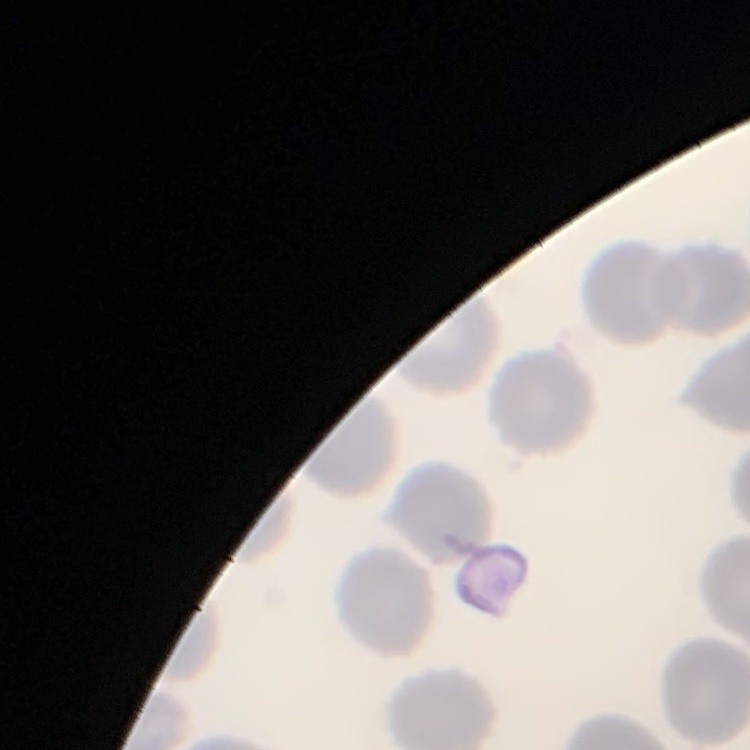

Summary:
  - Erythrocyte morphology: no rouleaux formation
  - Preparation: thin blood smear
  - Image type: one tile cut from a larger photomicrograph
  - Stain: Field's or Giemsa